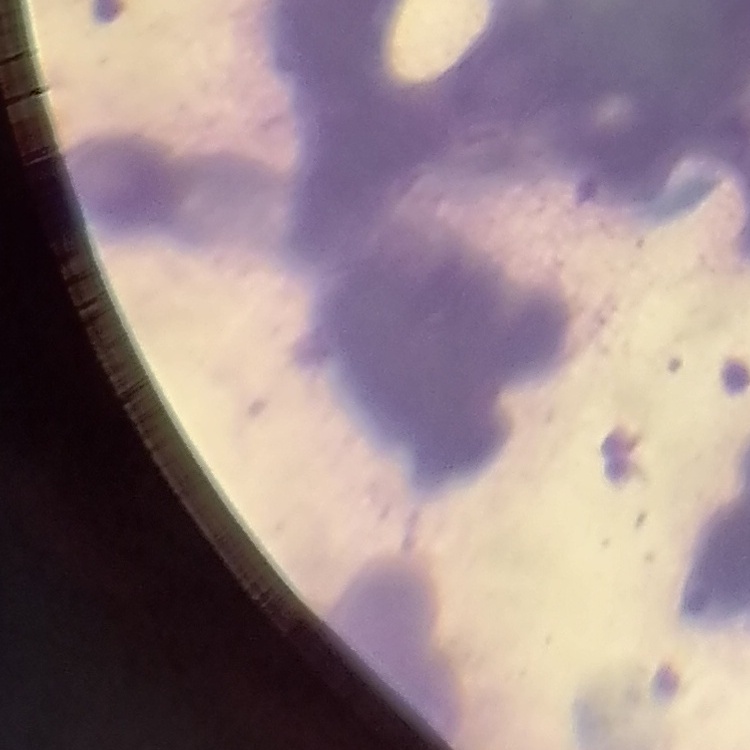 The red blood cells show rouleaux formation. Thin blood smear. One tile cut from a larger photomicrograph. Stained with either Field's or Giemsa.